Comment on the morphology of the erythrocytes.
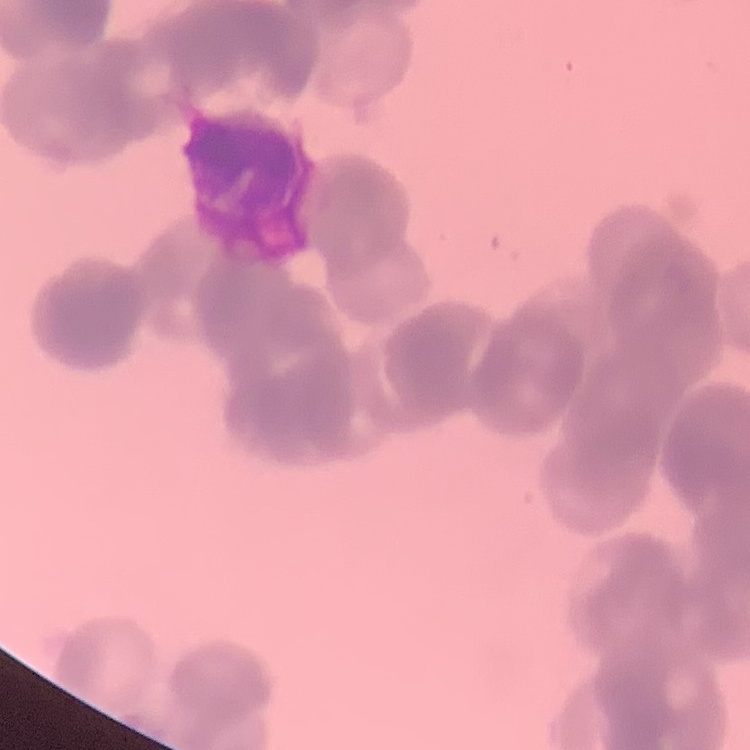

Rouleaux formation.

Summary:
  - Image type: one tile cut from a larger photomicrograph
  - Stain: Field's or Giemsa
  - Preparation: thin peripheral smear